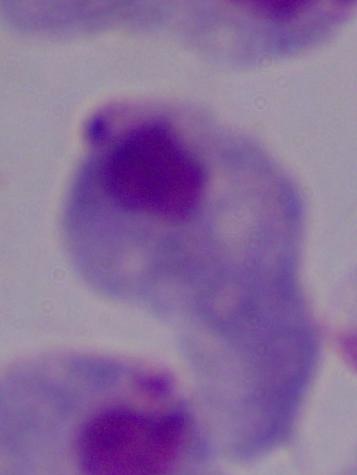
Summary:
  - Magnification: 1000x
  - Modality: photomicrograph
  - Identification: trichomonad